Identify the parasite.
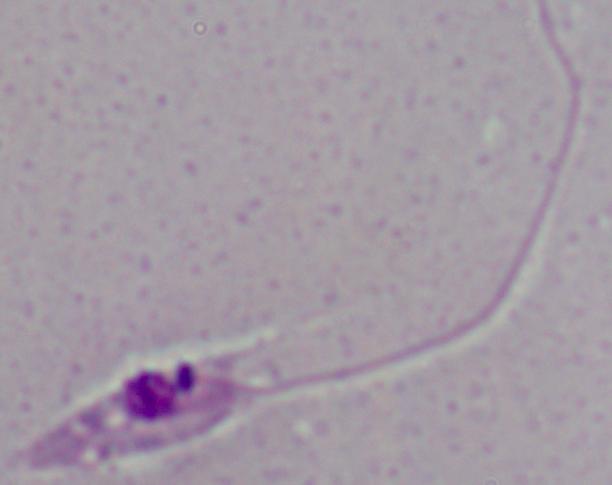
This is Leishmania.

Summary:
  - Magnification: 1000x
  - Modality: micrograph